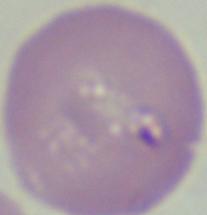
Summary:
  - Magnification: 1000x
  - Identification: Babesia
  - Modality: photomicrograph